Give the position of every malaria parasite.
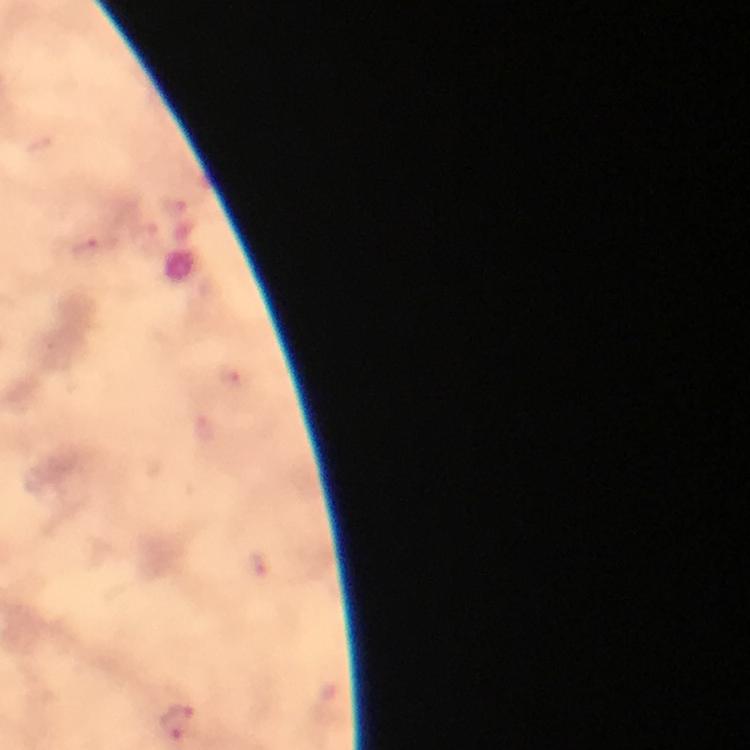
Approximate centers as {x, y} in pixels.
Malaria parasites: {89, 247}, {178, 723}.

Summary:
  - Capture: smartphone photograph through a microscope
  - Magnification: 100x
  - Stain: Giemsa
  - Context: from a diagnostic examination for malaria
  - Cropped from: one field of view
  - Preparation: thick smear
  - Image size: 750×750 pixels
  - Immersion oil: used